Describe the morphology of the red blood cells.
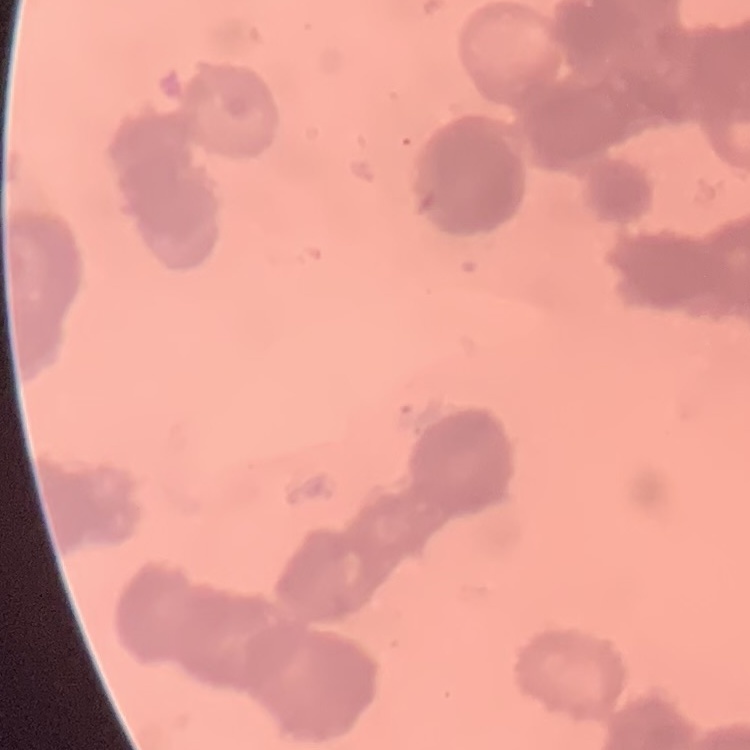
Rouleaux formation.

preparation = thin peripheral smear
stain = Field's or Giemsa
image type = square crop of a larger photomicrograph